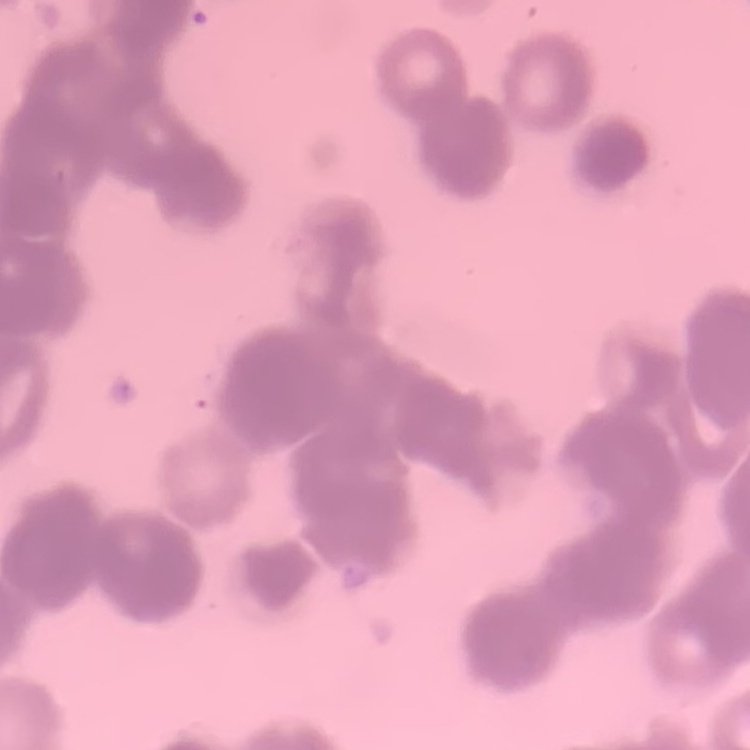
Summary:
  - Erythrocyte morphology: rouleaux formation
  - Stain: Field's or Giemsa
  - Preparation: thin peripheral smear
  - Image type: one tile cut from a larger photomicrograph